Classify this cell by malaria status.
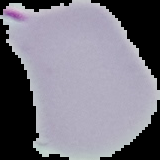

Parasitized.

image_type: segmented cell region with the area outside set to black
preparation: thin blood smear
image_size: 160×160 pixels